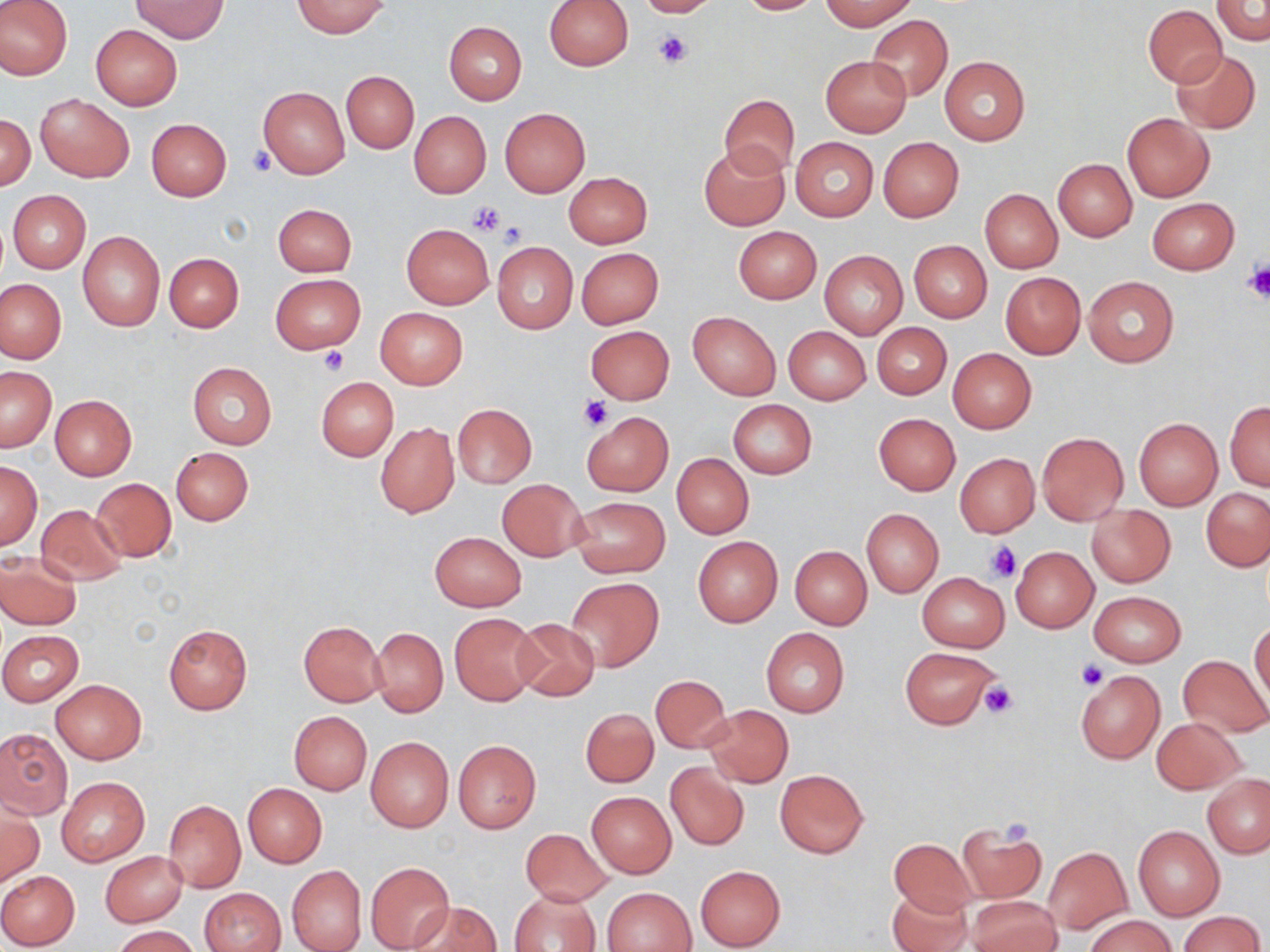
Approximate bounding boxes as (x1, y1, x2, y2) in pixels. Platelet locations: (654, 29, 690, 68), (247, 145, 276, 176), (468, 201, 506, 236), (495, 223, 527, 250), (1243, 262, 1270, 303), (317, 346, 349, 375), (580, 396, 611, 431), (984, 539, 1021, 583), (1075, 660, 1108, 691), (977, 681, 1018, 718), (996, 818, 1037, 847). Uninfected red blood cell locations: (1, 0, 73, 80), (634, 0, 720, 17), (735, 0, 826, 15), (819, 0, 918, 30), (130, 1, 229, 41), (291, 1, 389, 37), (545, 1, 634, 71), (1211, 1, 1270, 44), (1143, 5, 1227, 87), (865, 14, 952, 102), (444, 21, 526, 104), (90, 25, 183, 110), (1171, 49, 1260, 133), (820, 54, 912, 138), (940, 56, 1030, 145), (342, 71, 418, 152), (258, 86, 349, 179), (36, 94, 134, 182), (719, 94, 799, 176), (499, 107, 590, 197), (409, 111, 491, 198), (1121, 112, 1215, 201), (1, 114, 35, 190), (146, 118, 231, 200), (791, 137, 879, 222), (877, 137, 965, 222), (699, 144, 788, 230), (1053, 158, 1137, 241), (563, 172, 652, 248), (980, 188, 1062, 272), (7, 190, 91, 273), (1148, 198, 1239, 274), (274, 204, 356, 276), (401, 224, 494, 309), (733, 225, 822, 303), (78, 232, 165, 330), (908, 240, 992, 323), (493, 243, 577, 332), (575, 247, 663, 328), (819, 249, 908, 340), (163, 251, 244, 331), (1000, 272, 1085, 358), (270, 274, 365, 353), (1083, 276, 1178, 368), (0, 277, 65, 364), (375, 308, 467, 388), (688, 311, 780, 399), (872, 323, 951, 400), (586, 326, 675, 405), (784, 326, 870, 404), (947, 348, 1037, 433), (186, 361, 278, 449), (1, 366, 56, 451), (316, 376, 398, 460), (49, 395, 136, 480), (727, 400, 816, 479), (1225, 400, 1269, 491), (452, 403, 537, 486), (581, 411, 673, 496), (874, 413, 960, 494), (1134, 418, 1222, 510), (376, 422, 458, 518), (1037, 431, 1128, 525), (170, 447, 254, 526), (672, 453, 754, 538), (955, 453, 1040, 537), (0, 459, 42, 550), (90, 478, 176, 563), (497, 479, 587, 561), (1202, 488, 1270, 571), (568, 496, 671, 578), (35, 503, 127, 584), (1086, 504, 1176, 587), (861, 508, 944, 597), (430, 531, 525, 611), (692, 536, 783, 627), (790, 545, 872, 629), (1011, 546, 1098, 632), (0, 553, 82, 630), (917, 572, 1010, 651), (568, 576, 663, 670), (1089, 591, 1185, 666), (449, 612, 541, 706), (509, 617, 601, 702), (298, 621, 385, 706), (1249, 621, 1269, 707), (163, 624, 252, 714), (370, 627, 448, 716), (760, 628, 850, 716), (0, 630, 83, 705), (899, 646, 1002, 729), (1178, 655, 1269, 737), (1074, 670, 1165, 764), (650, 675, 732, 753), (50, 679, 147, 764), (704, 704, 793, 787), (581, 708, 658, 787), (288, 711, 372, 795), (1151, 717, 1244, 794), (0, 728, 72, 818), (366, 736, 454, 832), (452, 740, 541, 833), (665, 761, 749, 851), (774, 769, 868, 858), (1202, 774, 1270, 858), (57, 777, 148, 865), (244, 784, 326, 867), (1176, 784, 1262, 884), (586, 791, 677, 878), (164, 799, 246, 892), (0, 804, 42, 888), (956, 824, 1046, 904), (1133, 825, 1224, 921), (519, 828, 611, 906), (890, 839, 974, 914), (1041, 846, 1133, 934), (100, 850, 186, 926), (365, 861, 455, 951), (287, 864, 366, 952), (694, 865, 786, 950), (0, 870, 80, 949), (604, 887, 696, 952), (887, 887, 972, 952), (201, 888, 286, 952), (511, 889, 601, 952), (968, 899, 1061, 952), (410, 901, 500, 952), (1178, 910, 1265, 951), (1085, 914, 1176, 952), (112, 926, 200, 952). Slide-level diagnosis: negative for blood parasites. One field of a larger specimen. Thin blood smear. Image is 1270×952 pixels. Light microscopy. May-Grünwald-Giemsa-stained preparation. 1000x magnification.